Give the extent of all Plasmodium falciparum-infected red blood cells.
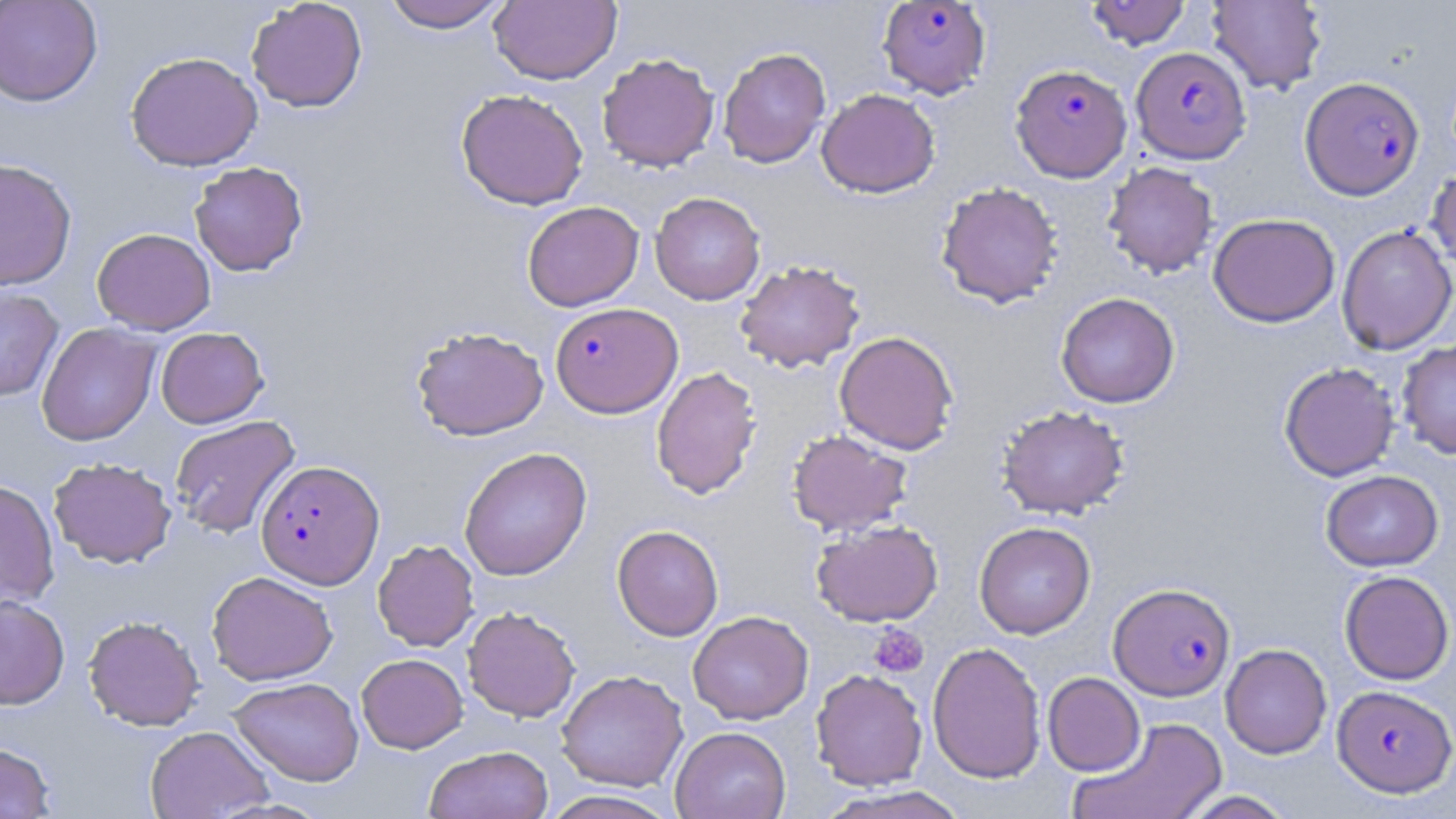
Approximate bounding boxes as (x1,y1)-(x2,y2) corner pairs in pixels.
Plasmodium falciparum-infected red blood cells (subset): (1131,46)-(1251,164), (1010,63)-(1132,183), (1299,76)-(1423,200), (550,301)-(682,418), (256,459)-(385,589), (1109,582)-(1235,701), (1332,684)-(1456,796).

Summary:
  - Uninfected red blood cell locations (subset): (246,0)-(368,113), (379,0)-(512,32), (1085,0)-(1191,51), (1206,0)-(1328,95), (0,1)-(103,107), (489,1)-(621,85), (717,47)-(831,168), (125,51)-(263,171), (597,53)-(720,172), (456,88)-(589,210), (816,88)-(940,198), (0,158)-(77,290), (189,161)-(308,276), (1103,161)-(1219,278), (1426,165)-(1456,276), (935,181)-(1063,309), (650,192)-(765,305), (522,201)-(644,311), (1208,213)-(1339,327), (1336,225)-(1456,355), (92,227)-(216,335), (734,259)-(866,373), (0,285)-(64,401), (1056,292)-(1180,408), (36,323)-(160,446), (411,326)-(549,441), (155,327)-(269,428), (834,330)-(959,455), (1397,338)-(1456,459), (1279,362)-(1400,481), (650,366)-(762,500), (996,405)-(1130,520), (168,415)-(301,539), (786,429)-(913,536), (459,446)-(592,581), (48,457)-(177,568), (1320,470)-(1443,571), (0,480)-(60,609), (811,519)-(943,627), (974,521)-(1095,638), (612,525)-(723,640), (372,539)-(479,652), (207,570)-(338,685), (1339,570)-(1455,685), (0,594)-(70,709), (462,606)-(581,722), (688,610)-(814,725), (83,615)-(205,731), (927,641)-(1046,783), (1220,643)-(1332,759), (356,653)-(467,753), (556,669)-(688,792), (810,669)-(928,790), (1042,672)-(1145,775), (228,677)-(364,786), (1069,717)-(1228,819), (145,725)-(274,818), (670,726)-(790,819), (0,742)-(56,818), (424,744)-(554,819), (817,786)-(971,819), (540,790)-(681,819), (1177,790)-(1298,818)
  - Platelet locations: (868,624)-(929,679)
  - Slide-level diagnosis: Plasmodium falciparum
  - Preparation: thin blood smear
  - Field of view: one of a larger specimen
  - Image size: 1456×819 pixels
  - Magnification: 1000x
  - Modality: light microscopy
  - Stain: May-Grünwald-Giemsa